Point out every Plasmodium parasite and every leukocyte.
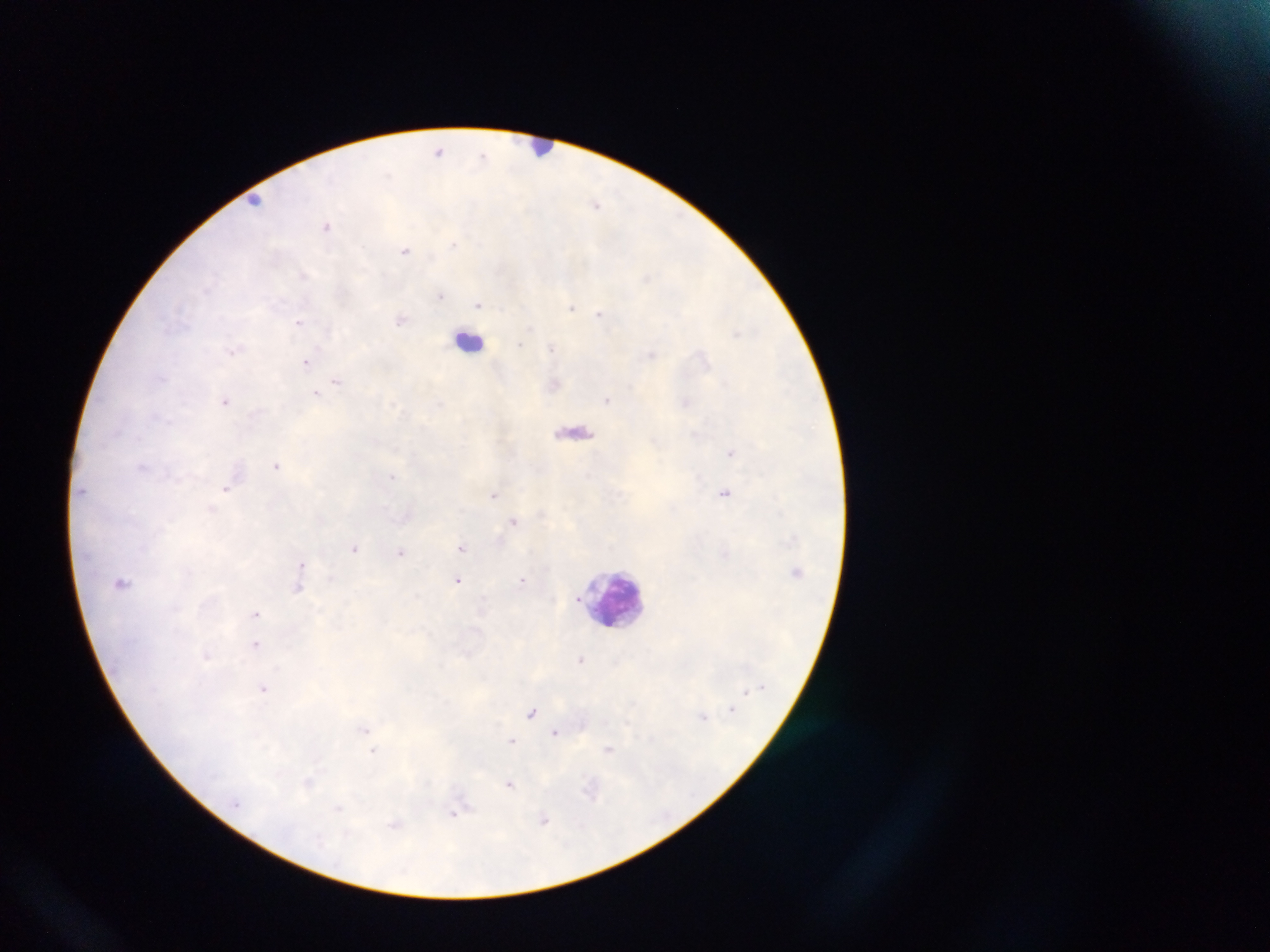

Approximate centers as {x, y} in pixels.
Plasmodium parasites: {439, 151}, {483, 155}, {597, 204}, {326, 225}, {453, 244}, {405, 250}, {302, 273}, {440, 295}, {478, 303}, {571, 307}, {599, 314}, {401, 320}, {298, 322}, {234, 351}, {651, 354}, {307, 361}, {336, 381}, {316, 393}, {225, 400}, {608, 400}, {731, 452}, {277, 465}, {392, 476}, {226, 488}, {724, 493}, {493, 494}, {211, 509}, {514, 521}, {355, 548}, {461, 548}, {401, 552}, {300, 565}, {523, 579}, {458, 580}, {298, 588}, {255, 613}, {257, 645}, {581, 659}, {263, 689}, {531, 713}, {365, 729}, {555, 732}, {513, 741}, {609, 749}, {373, 751}, {510, 784}, {591, 789}, {455, 812}, {545, 820}, {395, 824}.
Leukocytes: {543, 147}, {251, 201}, {469, 341}, {615, 597}.

One field of view. Thick blood film. Photographed through a microscope with a mobile-phone camera. Collected in Ghana. Image is 1270×952 pixels.